Give the location of every parasitized red blood cell.
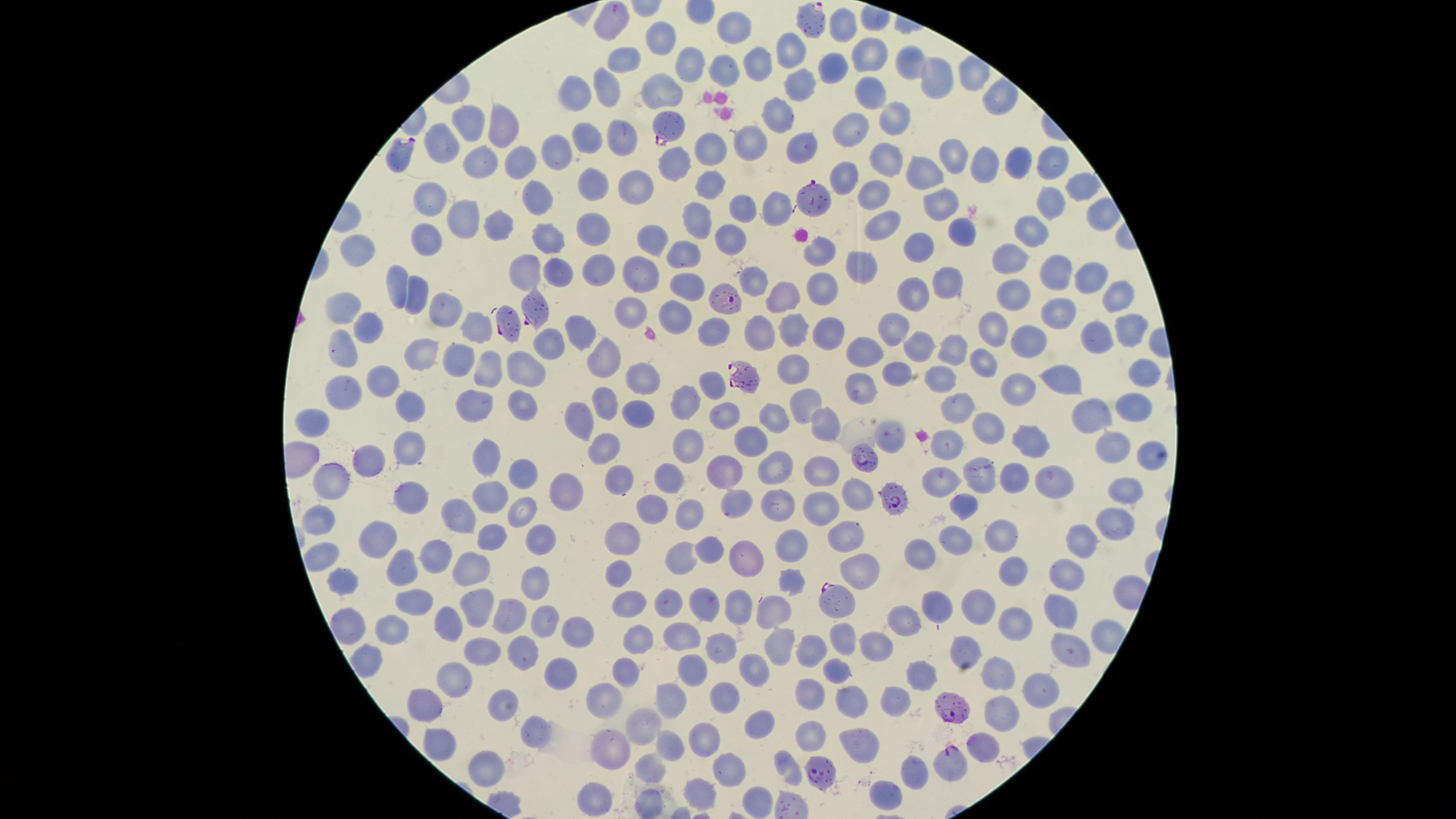
Approximate marker points, in pixels from the top-left corner.
Parasitized red blood cells: (x=812, y=16), (x=668, y=125), (x=403, y=151), (x=813, y=196), (x=722, y=298), (x=536, y=309), (x=507, y=320), (x=742, y=376), (x=863, y=458), (x=893, y=498), (x=833, y=599), (x=951, y=706), (x=950, y=765), (x=816, y=767).

Approximate marker points, in pixels from the top-left corner.
Summary:
  - Uninfected red blood cells: (x=613, y=22), (x=844, y=26), (x=732, y=27), (x=663, y=37), (x=790, y=49), (x=869, y=56), (x=687, y=58), (x=628, y=62), (x=761, y=63), (x=907, y=64), (x=727, y=67), (x=840, y=70), (x=800, y=79), (x=932, y=81), (x=660, y=83), (x=609, y=86), (x=871, y=89), (x=580, y=92), (x=992, y=94), (x=778, y=111), (x=891, y=114), (x=468, y=121), (x=503, y=121), (x=593, y=132), (x=619, y=133), (x=859, y=133), (x=754, y=138), (x=445, y=142), (x=804, y=146), (x=704, y=151), (x=559, y=153), (x=951, y=153), (x=883, y=158), (x=1014, y=158), (x=1050, y=160), (x=487, y=161), (x=671, y=162), (x=977, y=162), (x=522, y=164), (x=921, y=175), (x=848, y=178), (x=709, y=179), (x=642, y=185), (x=1080, y=186), (x=598, y=188), (x=540, y=194), (x=431, y=197), (x=872, y=198), (x=742, y=204), (x=937, y=205), (x=778, y=206), (x=1050, y=209), (x=696, y=215), (x=461, y=220), (x=882, y=225), (x=594, y=226), (x=961, y=233), (x=1032, y=233), (x=728, y=234), (x=548, y=237), (x=643, y=237), (x=421, y=240), (x=684, y=247), (x=821, y=248), (x=918, y=249), (x=363, y=252), (x=1005, y=255), (x=645, y=266), (x=861, y=267), (x=526, y=269), (x=599, y=270), (x=1054, y=271), (x=565, y=273), (x=1090, y=274), (x=947, y=277), (x=757, y=279), (x=396, y=282), (x=691, y=282), (x=418, y=288), (x=822, y=291), (x=914, y=292), (x=784, y=294), (x=1018, y=295), (x=1115, y=295), (x=443, y=306), (x=345, y=309), (x=1057, y=309), (x=675, y=314), (x=630, y=316), (x=1133, y=320), (x=992, y=321), (x=758, y=327), (x=895, y=328), (x=475, y=329), (x=577, y=330), (x=790, y=331), (x=370, y=332), (x=711, y=333), (x=832, y=334), (x=1032, y=336), (x=1101, y=336), (x=549, y=340), (x=428, y=343), (x=920, y=344), (x=345, y=347), (x=956, y=347), (x=605, y=349), (x=868, y=354), (x=461, y=355), (x=981, y=359), (x=485, y=367), (x=522, y=367), (x=799, y=367), (x=1144, y=371), (x=644, y=374), (x=897, y=374), (x=934, y=374), (x=1068, y=376), (x=712, y=379), (x=378, y=380), (x=861, y=385), (x=348, y=387), (x=1016, y=389), (x=686, y=396), (x=520, y=397), (x=475, y=399), (x=806, y=399), (x=605, y=401), (x=642, y=404), (x=956, y=407), (x=1129, y=408), (x=403, y=409), (x=724, y=412), (x=776, y=412), (x=580, y=418), (x=824, y=418), (x=1092, y=418), (x=990, y=430), (x=755, y=440), (x=1028, y=441), (x=1113, y=442), (x=690, y=446), (x=602, y=447), (x=952, y=447), (x=413, y=449), (x=1151, y=455), (x=486, y=460), (x=376, y=462), (x=523, y=469), (x=771, y=469), (x=730, y=472), (x=824, y=473), (x=942, y=477), (x=977, y=477), (x=625, y=479), (x=674, y=479), (x=1013, y=480), (x=1058, y=481), (x=567, y=486), (x=339, y=489), (x=1127, y=490), (x=493, y=492), (x=858, y=492), (x=413, y=493), (x=737, y=499), (x=776, y=503), (x=529, y=504), (x=963, y=505), (x=648, y=508), (x=689, y=508), (x=819, y=509), (x=1113, y=517), (x=323, y=518), (x=460, y=520), (x=1004, y=531), (x=377, y=532), (x=840, y=534), (x=627, y=535), (x=957, y=536), (x=498, y=538), (x=543, y=540), (x=791, y=543), (x=1083, y=544), (x=707, y=548), (x=680, y=554), (x=749, y=554), (x=928, y=555), (x=444, y=559), (x=405, y=561), (x=469, y=563), (x=861, y=565), (x=1009, y=569), (x=618, y=573), (x=1070, y=574), (x=344, y=581), (x=536, y=581), (x=791, y=581), (x=666, y=599), (x=629, y=600), (x=982, y=601), (x=737, y=602), (x=412, y=603), (x=699, y=603), (x=473, y=606), (x=941, y=607), (x=1060, y=611), (x=773, y=614), (x=506, y=619), (x=543, y=620), (x=1014, y=620), (x=906, y=623), (x=455, y=624), (x=350, y=626), (x=394, y=626), (x=577, y=627), (x=682, y=630), (x=844, y=633), (x=641, y=637), (x=776, y=641), (x=876, y=642), (x=810, y=644), (x=964, y=645), (x=720, y=647), (x=520, y=648), (x=1073, y=648), (x=481, y=649), (x=685, y=667), (x=997, y=668), (x=567, y=669), (x=747, y=669), (x=630, y=671), (x=927, y=672), (x=835, y=673), (x=457, y=675), (x=1038, y=686), (x=721, y=693), (x=610, y=696), (x=669, y=699), (x=809, y=699), (x=857, y=701), (x=901, y=701), (x=430, y=706), (x=497, y=706), (x=1001, y=710), (x=761, y=716), (x=645, y=727), (x=537, y=734), (x=707, y=735), (x=809, y=738), (x=444, y=743), (x=612, y=743), (x=984, y=744), (x=669, y=745), (x=868, y=745), (x=481, y=760), (x=724, y=767), (x=787, y=767), (x=645, y=772), (x=910, y=776), (x=886, y=790), (x=699, y=796), (x=753, y=798), (x=600, y=799)
  - Species: Plasmodium falciparum
  - Capture: smartphone photograph through the microscope eyepiece
  - Preparation: thin smear of blood
  - Visible region: circular
  - Stain: Giemsa
  - Field of view: single
  - Image size: 1456×819 pixels